Give the position of every Plasmodium parasite.
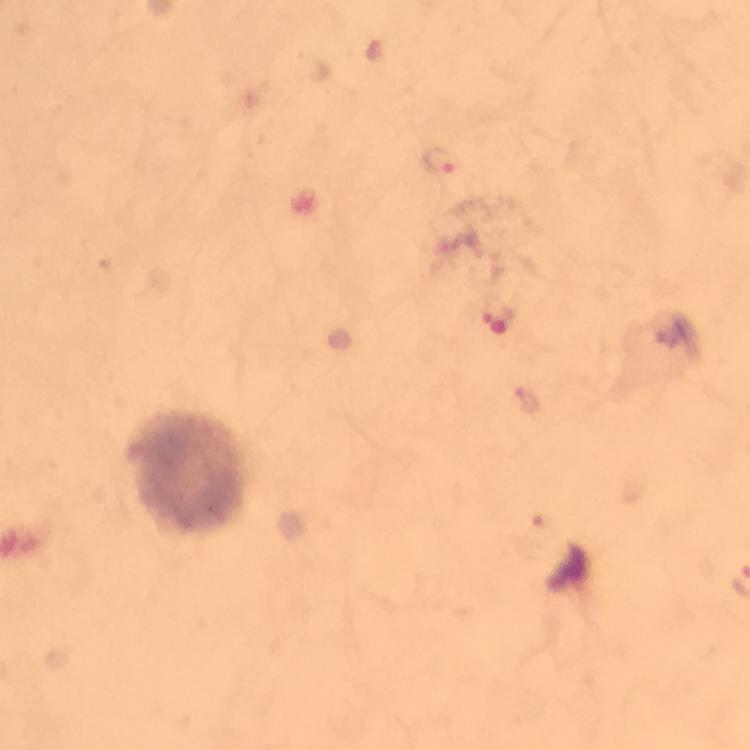
Approximate centers as [x, y] in pixels.
Plasmodium parasites: [439, 161], [495, 321].

Summary:
  - Immersion oil: applied
  - Stain: Giemsa
  - Magnification: 100x
  - Cropped from: a single field of view
  - Image size: 750×750 pixels
  - Context: from a diagnostic examination for malaria
  - Preparation: thick blood smear
  - Capture: smartphone photograph through a microscope